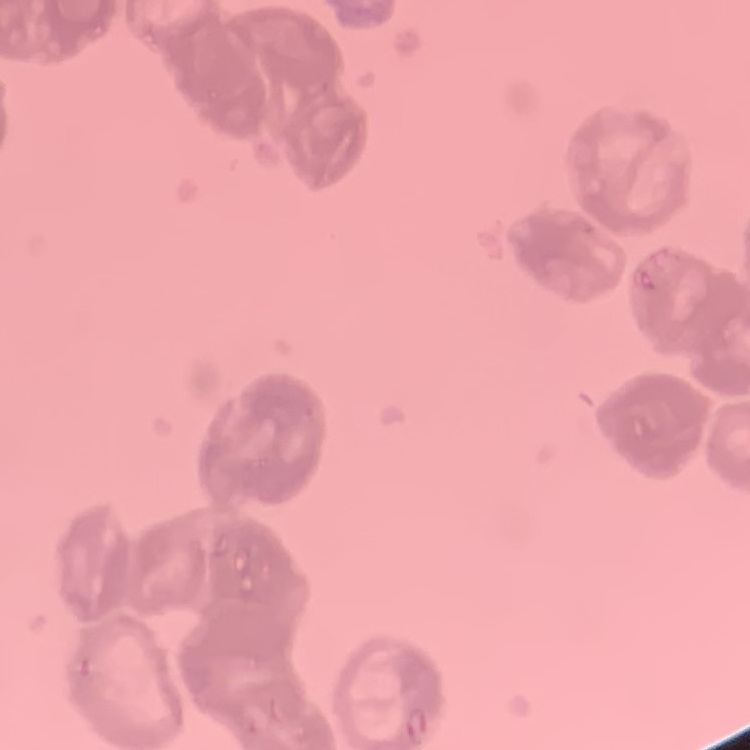
Summary:
  - Red blood cell morphology: rouleaux formation
  - Stain: Field's or Giemsa
  - Preparation: thin peripheral smear
  - Image type: square crop of a larger photomicrograph